Outline each blood parasite and name the species.
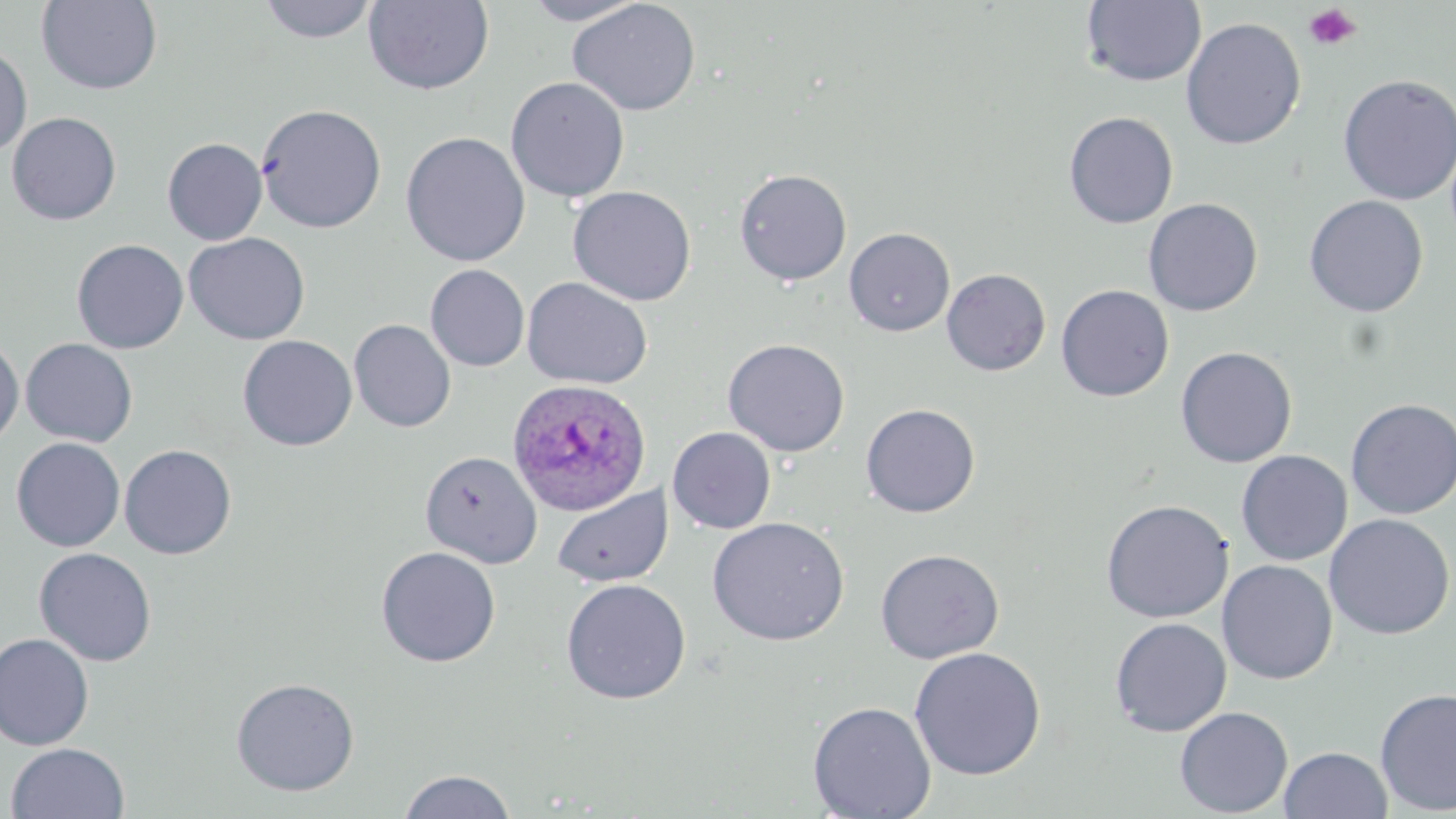
Approximate bounding boxes as [x1, y1, x2, y2] in pixels.
Plasmodium ovale-infected red blood cells: [507, 378, 653, 516].
No Plasmodium falciparum, Plasmodium malariae, Plasmodium vivax, Babesia divergens, or Trypanosoma brucei observed.

{
  "slide_level_diagnosis": "Plasmodium ovale",
  "image_size": "1456×819 pixels",
  "magnification": "1000x",
  "field_of_view": "one of a larger specimen",
  "platelet_locations": "approximate bounding boxes as [x1, y1, x2, y2] in pixels: [1302, 4, 1362, 51]",
  "uninfected_red_blood_cell_locations": "approximate bounding boxes as [x1, y1, x2, y2] in pixels: [256, 0, 380, 44], [363, 0, 494, 95], [519, 0, 650, 26], [567, 0, 701, 116], [1081, 0, 1206, 87], [36, 1, 163, 94], [1181, 17, 1306, 150], [0, 43, 32, 157], [1337, 74, 1456, 206], [505, 76, 630, 202], [255, 104, 387, 233], [6, 112, 122, 226], [1063, 112, 1179, 229], [400, 132, 530, 266], [162, 137, 268, 245], [734, 168, 852, 286], [567, 185, 697, 307], [1304, 195, 1429, 317], [1143, 198, 1263, 316], [844, 227, 955, 337], [183, 233, 310, 345], [71, 239, 189, 354], [425, 264, 530, 372], [940, 268, 1051, 376], [521, 276, 653, 390], [1056, 284, 1174, 402], [349, 318, 456, 433], [0, 334, 24, 452], [237, 335, 358, 452], [20, 338, 138, 447], [722, 338, 850, 457], [1175, 346, 1297, 468], [1345, 398, 1456, 519], [861, 403, 981, 517], [667, 427, 776, 534], [11, 437, 126, 552], [119, 443, 237, 559], [420, 450, 542, 568], [1236, 450, 1353, 566], [551, 485, 673, 588], [1100, 499, 1234, 623], [1324, 513, 1455, 640], [707, 517, 850, 646], [375, 546, 501, 668], [33, 547, 157, 666], [874, 548, 1004, 664], [1217, 559, 1338, 684], [560, 578, 691, 705], [1109, 617, 1232, 737], [0, 632, 95, 751], [909, 646, 1047, 781], [230, 677, 359, 797], [1374, 686, 1456, 815], [807, 701, 937, 818], [1174, 706, 1293, 817], [5, 741, 130, 819], [1278, 746, 1393, 819], [398, 769, 518, 818]",
  "stain": "May-Grünwald-Giemsa",
  "modality": "optical microscopy",
  "preparation": "thin blood smear"
}